Locate every Plasmodium vivax-infected red blood cell.
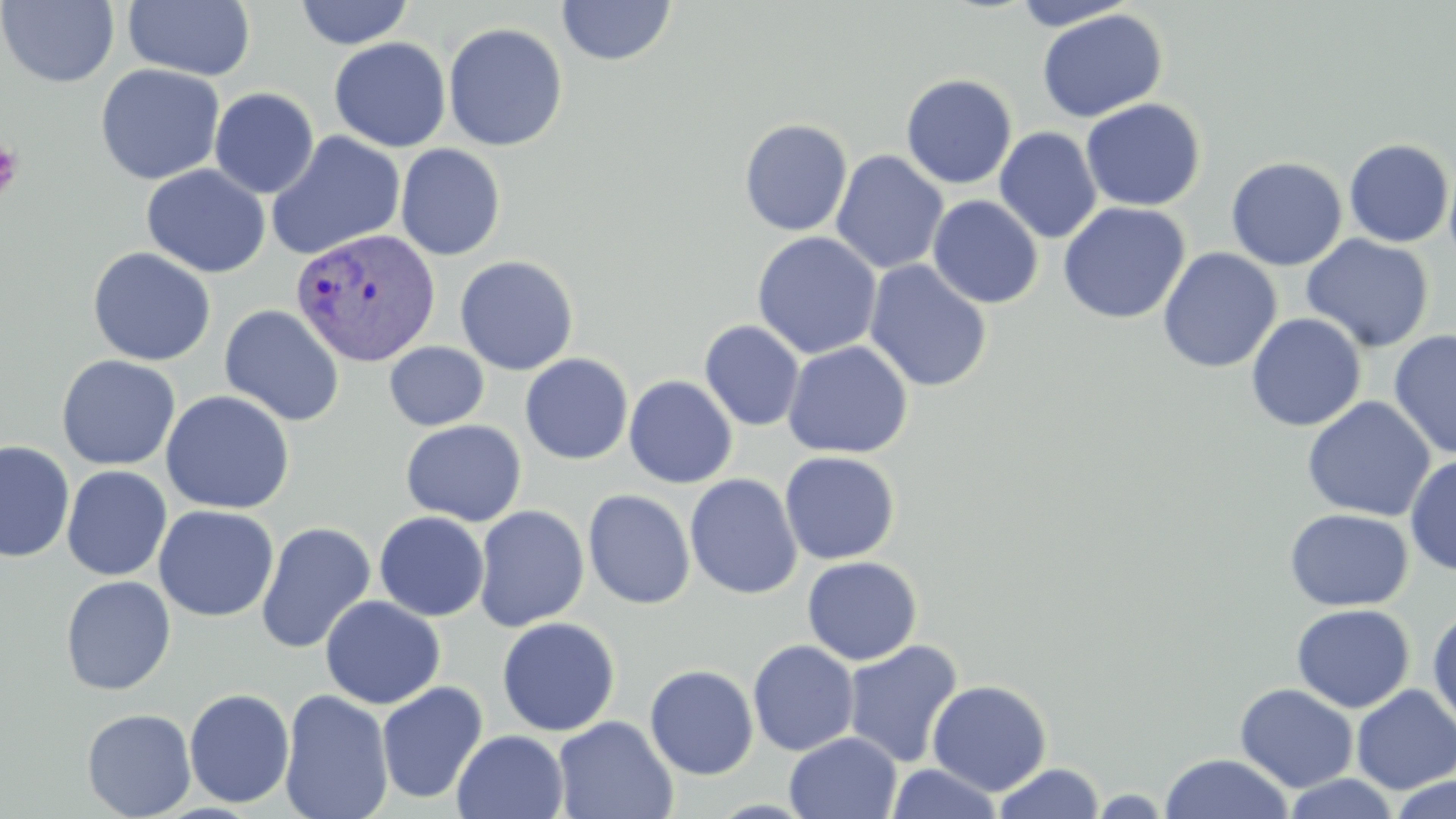

Approximate bounding boxes as named x1/y1/x2/y2 corners in pixels.
Plasmodium vivax-infected red blood cells: (x1=291, y1=226, x2=441, y2=367).

Summary:
  - Uninfected red blood cell locations: (x1=1, y1=0, x2=119, y2=88), (x1=123, y1=0, x2=256, y2=81), (x1=293, y1=1, x2=415, y2=49), (x1=557, y1=1, x2=676, y2=66), (x1=1007, y1=1, x2=1140, y2=30), (x1=1036, y1=8, x2=1167, y2=123), (x1=443, y1=22, x2=568, y2=152), (x1=328, y1=37, x2=451, y2=152), (x1=95, y1=63, x2=226, y2=185), (x1=900, y1=74, x2=1018, y2=189), (x1=209, y1=88, x2=320, y2=199), (x1=1080, y1=98, x2=1206, y2=212), (x1=738, y1=118, x2=853, y2=237), (x1=994, y1=127, x2=1102, y2=244), (x1=265, y1=130, x2=406, y2=262), (x1=1343, y1=138, x2=1455, y2=248), (x1=395, y1=143, x2=506, y2=261), (x1=830, y1=150, x2=949, y2=275), (x1=1226, y1=157, x2=1348, y2=270), (x1=141, y1=164, x2=271, y2=278), (x1=927, y1=194, x2=1044, y2=309), (x1=1058, y1=201, x2=1191, y2=324), (x1=752, y1=231, x2=882, y2=360), (x1=1300, y1=234, x2=1434, y2=353), (x1=87, y1=247, x2=217, y2=366), (x1=1157, y1=247, x2=1282, y2=373), (x1=455, y1=255, x2=579, y2=375), (x1=863, y1=259, x2=993, y2=392), (x1=219, y1=304, x2=345, y2=426), (x1=1246, y1=313, x2=1366, y2=432), (x1=699, y1=320, x2=805, y2=431), (x1=1388, y1=329, x2=1456, y2=460), (x1=782, y1=340, x2=913, y2=459), (x1=384, y1=342, x2=489, y2=431), (x1=519, y1=353, x2=634, y2=466), (x1=56, y1=354, x2=181, y2=470), (x1=623, y1=375, x2=738, y2=489), (x1=160, y1=389, x2=295, y2=514), (x1=1301, y1=396, x2=1435, y2=521), (x1=400, y1=419, x2=527, y2=526), (x1=0, y1=441, x2=75, y2=562), (x1=779, y1=451, x2=901, y2=565), (x1=1404, y1=455, x2=1456, y2=576), (x1=61, y1=465, x2=172, y2=581), (x1=684, y1=474, x2=802, y2=600), (x1=583, y1=489, x2=696, y2=609), (x1=153, y1=504, x2=279, y2=623), (x1=474, y1=505, x2=590, y2=632), (x1=1284, y1=508, x2=1412, y2=611), (x1=374, y1=512, x2=490, y2=621), (x1=255, y1=521, x2=376, y2=654), (x1=802, y1=556, x2=922, y2=665), (x1=60, y1=575, x2=176, y2=696), (x1=320, y1=595, x2=445, y2=710), (x1=1291, y1=604, x2=1415, y2=713), (x1=1427, y1=606, x2=1456, y2=731), (x1=496, y1=617, x2=620, y2=736), (x1=841, y1=639, x2=964, y2=767), (x1=747, y1=640, x2=860, y2=756), (x1=644, y1=664, x2=759, y2=780), (x1=926, y1=679, x2=1052, y2=795), (x1=376, y1=680, x2=488, y2=805), (x1=1235, y1=684, x2=1358, y2=792), (x1=1352, y1=684, x2=1456, y2=794), (x1=184, y1=688, x2=295, y2=809), (x1=279, y1=689, x2=394, y2=819), (x1=81, y1=708, x2=196, y2=819), (x1=552, y1=715, x2=678, y2=819), (x1=452, y1=730, x2=570, y2=819), (x1=783, y1=731, x2=902, y2=819), (x1=1158, y1=753, x2=1295, y2=818), (x1=992, y1=762, x2=1105, y2=819), (x1=887, y1=763, x2=1003, y2=819), (x1=1283, y1=773, x2=1401, y2=818), (x1=1388, y1=776, x2=1456, y2=819), (x1=1085, y1=789, x2=1176, y2=817)
  - Platelet locations: (x1=0, y1=141, x2=24, y2=202)
  - Slide-level diagnosis: Plasmodium vivax
  - Preparation: thin blood film
  - Field of view: single
  - Stain: May-Grünwald-Giemsa
  - Modality: optical microscopy
  - Image size: 1456×819 pixels
  - Magnification: 1000x